Name the cell type shown.
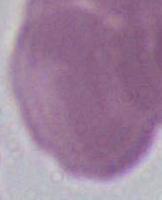

This is an erythrocyte.

Summary:
  - Magnification: 1000x
  - Modality: micrograph